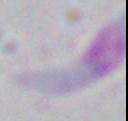

magnification = 1000x
identification = Toxoplasma gondii
modality = photomicrograph